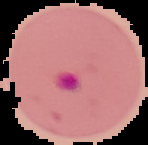

Summary:
  - Image type: cell region segmented out of the field of view; surrounding area masked to black
  - Preparation: thin blood film
  - Image size: 148×145 pixels
  - Result: Plasmodium parasites detected